Give the extent of all white blood cells.
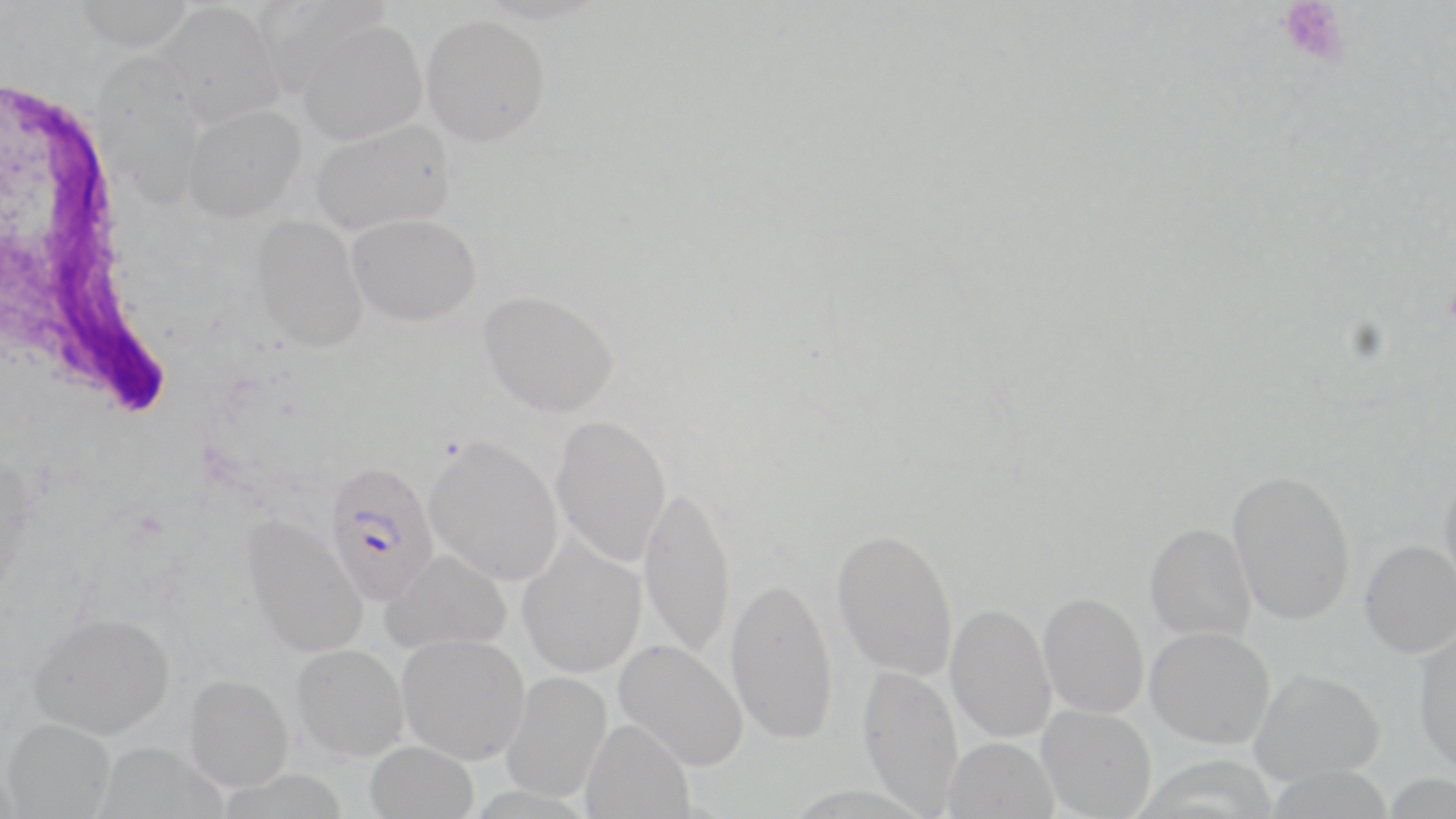
Approximate bounding boxes as named x1/y1/x2/y2 corners in pixels.
White blood cells: (x1=5, y1=72, x2=177, y2=425).

Summary:
  - Platelet locations: (x1=1276, y1=1, x2=1350, y2=69)
  - Plasmodium falciparum-infected red blood cell locations: (x1=323, y1=460, x2=440, y2=605)
  - Uninfected red blood cell locations: (x1=75, y1=0, x2=194, y2=51), (x1=254, y1=1, x2=390, y2=96), (x1=156, y1=2, x2=283, y2=128), (x1=421, y1=15, x2=550, y2=146), (x1=296, y1=18, x2=425, y2=145), (x1=95, y1=53, x2=206, y2=209), (x1=183, y1=104, x2=305, y2=222), (x1=311, y1=120, x2=454, y2=235), (x1=251, y1=214, x2=368, y2=352), (x1=347, y1=214, x2=481, y2=325), (x1=479, y1=289, x2=619, y2=417), (x1=551, y1=413, x2=672, y2=566), (x1=424, y1=435, x2=564, y2=585), (x1=1227, y1=468, x2=1357, y2=626), (x1=1439, y1=470, x2=1456, y2=595), (x1=639, y1=484, x2=737, y2=658), (x1=241, y1=513, x2=368, y2=659), (x1=1145, y1=522, x2=1256, y2=643), (x1=831, y1=527, x2=959, y2=680), (x1=517, y1=533, x2=647, y2=678), (x1=1359, y1=539, x2=1456, y2=658), (x1=381, y1=549, x2=512, y2=654), (x1=725, y1=575, x2=838, y2=742), (x1=1038, y1=591, x2=1150, y2=719), (x1=945, y1=602, x2=1056, y2=743), (x1=27, y1=611, x2=175, y2=739), (x1=1145, y1=626, x2=1276, y2=748), (x1=1413, y1=626, x2=1456, y2=777), (x1=397, y1=633, x2=530, y2=764), (x1=614, y1=639, x2=748, y2=770), (x1=291, y1=644, x2=408, y2=760), (x1=857, y1=664, x2=964, y2=816), (x1=1250, y1=668, x2=1385, y2=785), (x1=501, y1=671, x2=612, y2=803), (x1=183, y1=675, x2=293, y2=791), (x1=1037, y1=704, x2=1156, y2=818), (x1=2, y1=718, x2=115, y2=818), (x1=580, y1=718, x2=695, y2=819), (x1=943, y1=736, x2=1059, y2=819), (x1=93, y1=741, x2=227, y2=818), (x1=365, y1=741, x2=479, y2=819)
  - Slide-level diagnosis: Plasmodium falciparum
  - Magnification: 1000x
  - Stain: May-Grünwald-Giemsa
  - Modality: optical microscopy
  - Field of view: one of a larger specimen
  - Image size: 1456×819 pixels
  - Preparation: thin blood smear